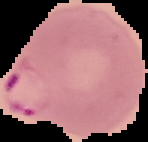
Result: Plasmodium parasites detected. Image is 148×142 pixels. Cell region segmented out of the field of view; the surrounding area is masked to black. From a thin blood film.